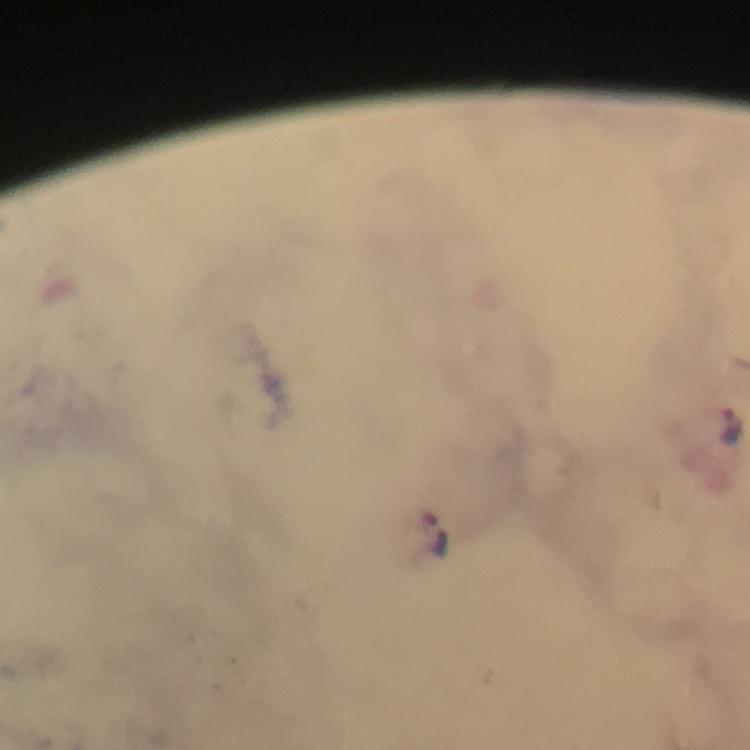

Approximate centers as [x, y] in pixels. Plasmodium parasite locations: [730, 426], [437, 533]. Giemsa-stained preparation. Cropped region of a single field of view. Image is 750×750 pixels. Immersion oil was used. From a diagnostic examination for malaria. At 100x magnification. Photographed with a smartphone mounted on the microscope. Thick blood film.